Locate every leukocyte (white blood cell).
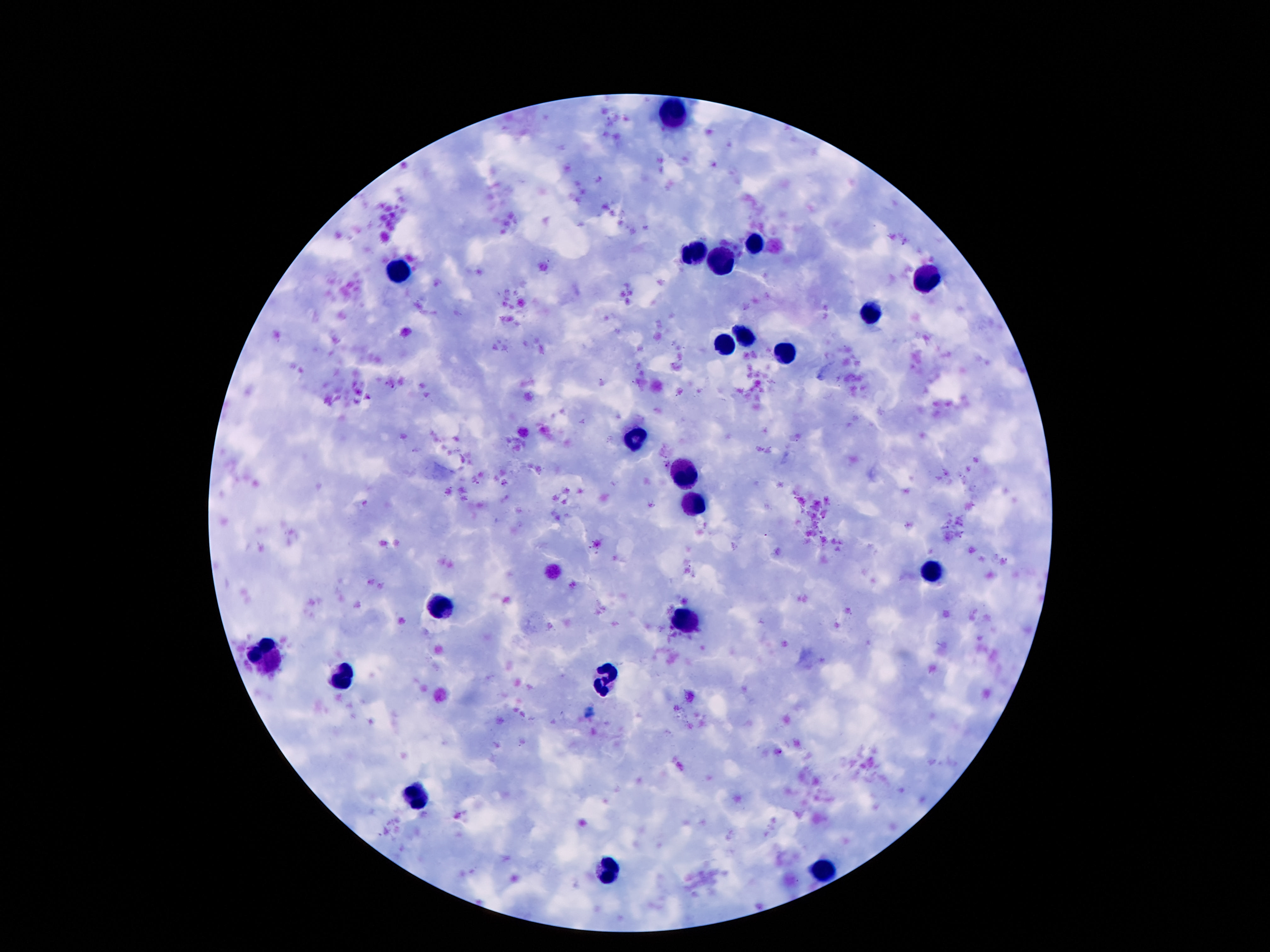
Approximate centers as [x, y] in pixels.
Leukocytes: [672, 115], [756, 245], [698, 253], [724, 262], [397, 273], [924, 281], [868, 311], [746, 337], [724, 345], [784, 355], [632, 440], [687, 475], [692, 505], [933, 573], [442, 607], [687, 620], [266, 657], [604, 676], [341, 677], [420, 797], [821, 869], [610, 872].

Photographed through the microscope eyepiece with a smartphone camera. Thick blood smear. Patient malaria status: negative. Single field of view. 100x magnification. Image is 1270×952 pixels. Giemsa stain.